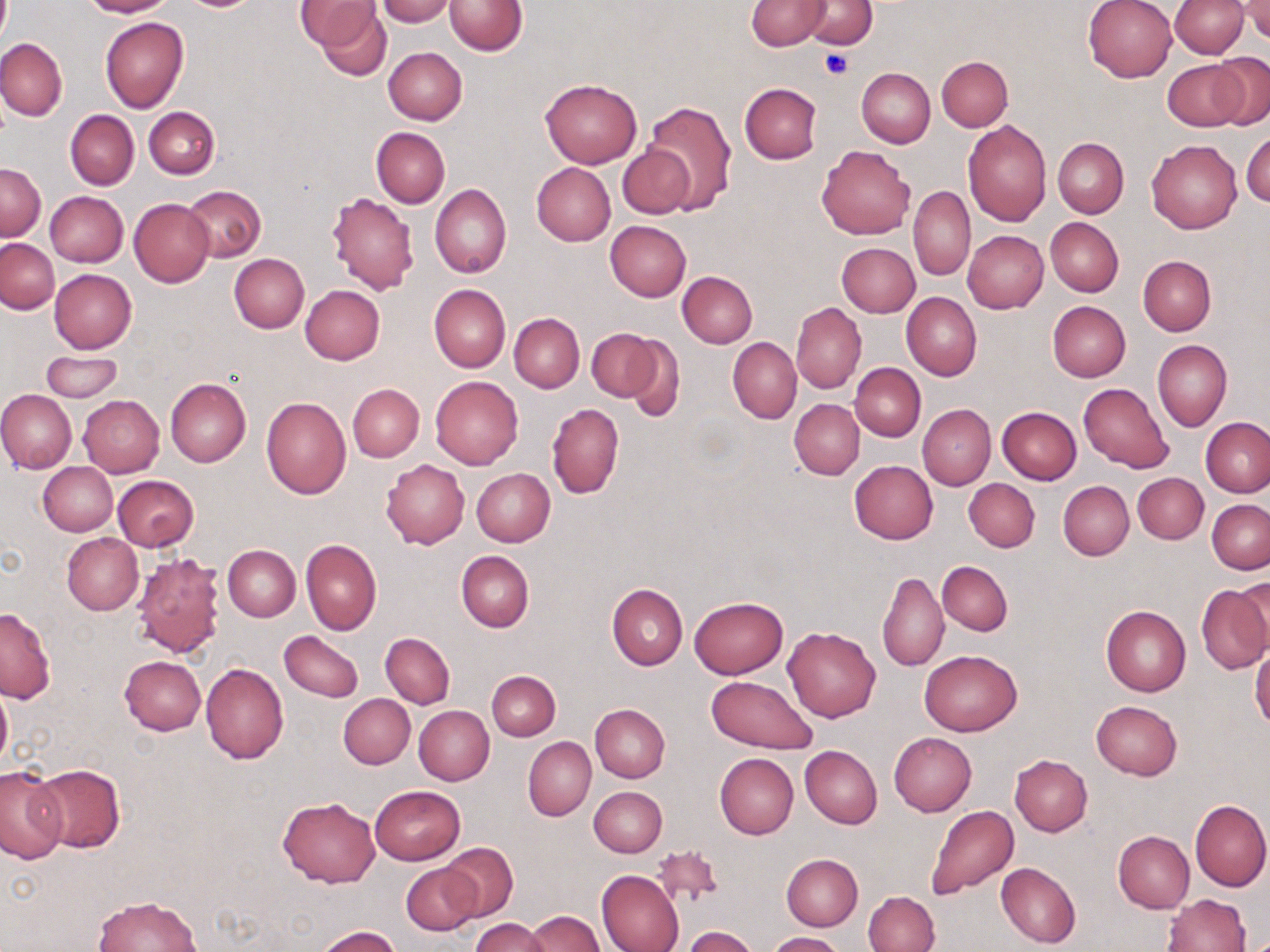
Approximate bounding boxes as (x1, y1, x2, y2) in pixels. Uninfected red blood cell locations: (82, 0, 174, 17), (377, 0, 455, 25), (745, 0, 831, 50), (800, 0, 877, 48), (1083, 0, 1177, 83), (1168, 0, 1249, 58), (1239, 0, 1270, 41), (303, 1, 390, 76), (446, 1, 527, 55), (100, 16, 188, 112), (0, 38, 67, 121), (383, 47, 466, 124), (1210, 53, 1269, 129), (936, 56, 1013, 130), (1162, 59, 1249, 132), (857, 68, 935, 147), (541, 79, 641, 168), (739, 83, 822, 164), (644, 101, 737, 211), (144, 107, 218, 179), (66, 110, 139, 189), (963, 119, 1051, 225), (371, 128, 449, 208), (1243, 129, 1270, 209), (1052, 137, 1128, 218), (1147, 139, 1241, 233), (618, 144, 698, 218), (817, 145, 916, 239), (1, 163, 46, 239), (532, 163, 615, 245), (430, 183, 511, 278), (184, 185, 266, 262), (909, 185, 976, 280), (44, 190, 129, 267), (326, 192, 418, 295), (130, 198, 214, 287), (1046, 217, 1123, 297), (604, 221, 691, 301), (963, 230, 1048, 313), (1, 238, 58, 314), (836, 243, 919, 316), (229, 253, 309, 333), (1138, 256, 1216, 335), (48, 270, 137, 353), (678, 272, 757, 348), (300, 284, 385, 364), (428, 284, 511, 373), (901, 292, 981, 382), (1047, 301, 1131, 381), (791, 303, 866, 392), (510, 313, 584, 393), (586, 328, 664, 403), (728, 337, 801, 423), (625, 338, 686, 421), (1153, 338, 1231, 432), (41, 350, 123, 403), (851, 364, 926, 441), (432, 376, 524, 469), (165, 378, 251, 467), (1078, 382, 1173, 473), (347, 384, 424, 461), (0, 390, 76, 473), (79, 395, 164, 476), (261, 397, 351, 499), (790, 400, 864, 478), (547, 403, 623, 499), (917, 404, 995, 491), (996, 407, 1081, 485), (1202, 417, 1270, 496), (381, 459, 469, 549), (849, 461, 938, 544), (38, 462, 117, 536), (471, 468, 554, 546), (1132, 472, 1208, 544), (113, 475, 198, 551), (964, 478, 1039, 552), (1058, 481, 1134, 560), (1207, 500, 1269, 573), (62, 533, 143, 614), (301, 539, 382, 636), (223, 544, 300, 621), (132, 551, 223, 660), (457, 551, 534, 632), (936, 561, 1013, 635), (878, 572, 948, 671), (1196, 583, 1270, 674), (606, 584, 686, 670), (688, 596, 788, 680), (1100, 605, 1191, 696), (1, 607, 56, 703), (782, 625, 881, 723), (280, 630, 363, 701), (381, 633, 454, 709), (1250, 647, 1270, 731), (919, 650, 1023, 736), (119, 655, 205, 734), (200, 662, 288, 764), (487, 671, 559, 741), (706, 675, 816, 755), (0, 684, 11, 771), (338, 694, 415, 769), (1090, 699, 1183, 780), (590, 703, 670, 782), (414, 705, 495, 785), (889, 733, 976, 816), (523, 737, 596, 821), (800, 746, 881, 828), (715, 753, 799, 840), (1010, 755, 1092, 837), (33, 763, 125, 853), (0, 766, 66, 862), (371, 785, 465, 864), (589, 786, 667, 856), (278, 796, 381, 888), (1189, 800, 1270, 892), (925, 805, 1019, 900), (1113, 830, 1194, 913), (439, 844, 518, 922), (652, 844, 724, 909), (781, 854, 862, 931), (995, 862, 1081, 948), (402, 863, 479, 935), (597, 870, 685, 952), (863, 891, 939, 952), (1162, 893, 1251, 952), (92, 895, 203, 952), (525, 910, 605, 951), (471, 918, 551, 952), (315, 925, 401, 952), (683, 926, 758, 952), (768, 932, 843, 952). Platelet locations: (821, 48, 853, 79). Slide-level diagnosis: negative for blood parasites. May-Grünwald-Giemsa stain. Optical microscopy. Captured at 1000x magnification. Image is 1270×952 pixels. Single field of view. Thin blood smear.